Classify this cell by malaria status.
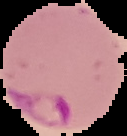
It is parasitized.

image_type: segmented cell region on a black background
preparation: thin blood film
image_size: 127×136 pixels